Locate every uninfected red blood cell.
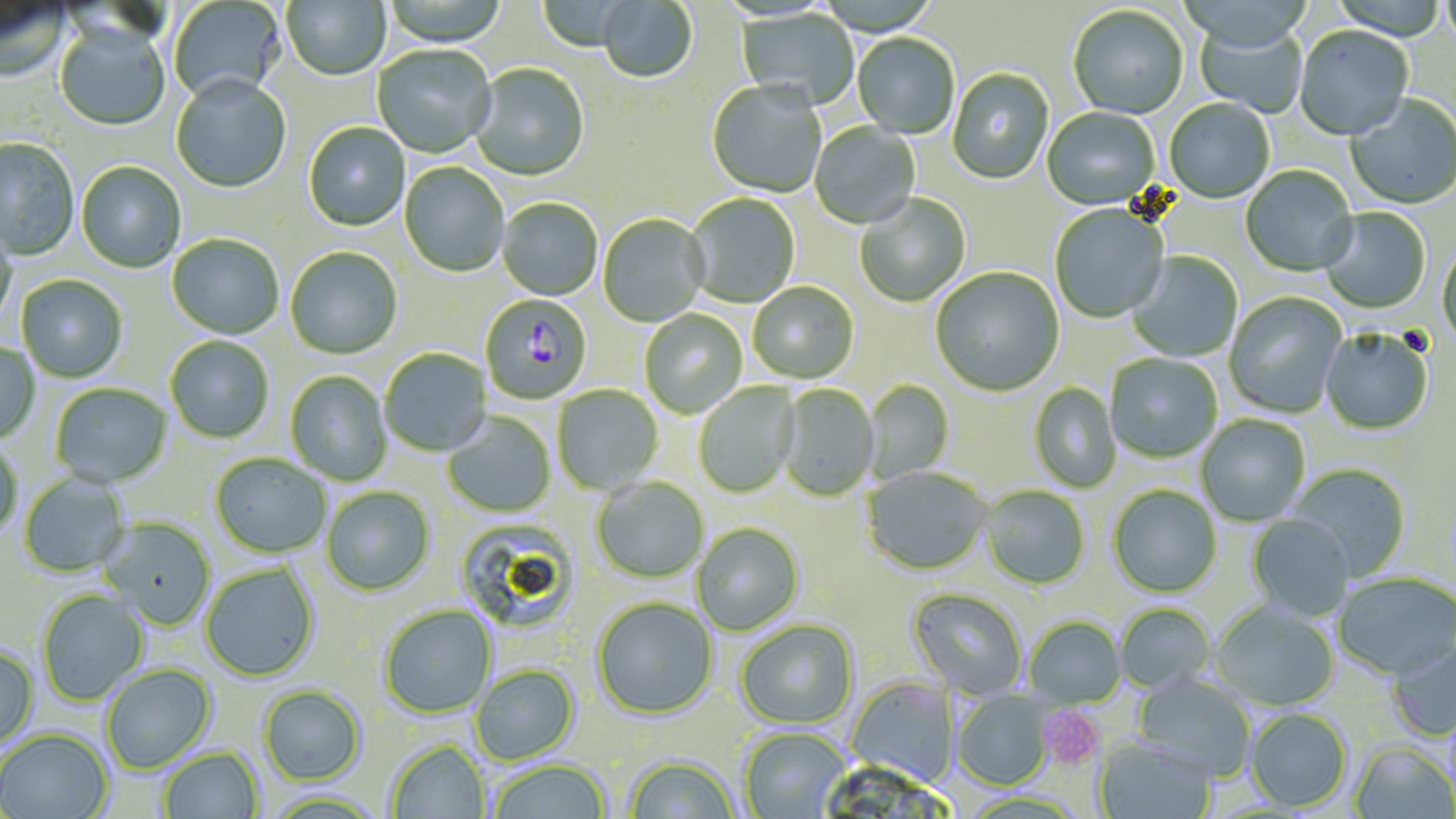

Approximate bounding boxes as (x1,y1)-(x2,y2) corner pairs in pixels.
Uninfected red blood cells: (281,0)-(390,82), (380,0)-(507,48), (536,0)-(640,53), (1440,0)-(1456,57), (1,1)-(72,84), (167,1)-(287,106), (597,1)-(698,85), (1067,6)-(1189,120), (735,9)-(859,110), (1191,22)-(1309,118), (53,26)-(170,132), (1294,26)-(1413,143), (852,34)-(959,139), (372,46)-(497,159), (469,65)-(589,182), (947,69)-(1054,185), (170,78)-(291,194), (706,82)-(827,199), (1345,95)-(1456,211), (1164,99)-(1275,204), (1042,108)-(1159,211), (809,122)-(921,230), (303,124)-(409,232), (0,139)-(79,262), (76,163)-(186,273), (400,163)-(509,277), (1240,167)-(1359,277), (684,194)-(800,309), (854,194)-(971,308), (497,199)-(602,301), (1050,205)-(1169,324), (1319,208)-(1431,314), (597,214)-(709,327), (0,220)-(17,327), (167,235)-(284,340), (1437,244)-(1456,351), (285,247)-(402,360), (1126,252)-(1242,363), (930,268)-(1064,397), (16,275)-(128,383), (748,282)-(859,384), (1224,292)-(1347,419), (639,309)-(747,418), (1320,329)-(1434,436), (164,336)-(274,444), (0,339)-(42,445), (379,348)-(491,457), (1104,353)-(1222,464), (285,371)-(393,486), (863,380)-(955,483), (693,382)-(800,498), (50,383)-(172,488), (1028,383)-(1121,493), (552,384)-(664,495), (777,384)-(880,501), (443,412)-(555,517), (1196,415)-(1310,526), (0,436)-(24,543), (210,453)-(331,558), (1289,464)-(1411,580), (861,466)-(991,575), (18,472)-(130,577), (592,478)-(709,583), (980,485)-(1090,589), (1108,485)-(1222,598), (321,486)-(435,596), (1246,515)-(1354,621), (98,516)-(216,630), (454,519)-(579,633), (691,523)-(804,635), (199,563)-(320,682), (1333,573)-(1455,680), (907,587)-(1028,700), (36,589)-(149,705), (592,596)-(718,720), (1210,602)-(1340,712), (379,604)-(497,718), (1114,604)-(1214,694), (1023,616)-(1127,709), (735,619)-(859,729), (1386,637)-(1456,741), (0,643)-(39,749), (100,664)-(217,774), (470,665)-(579,765), (1132,672)-(1256,780), (845,676)-(958,788), (257,685)-(367,786), (952,689)-(1055,791), (1245,708)-(1353,813), (739,727)-(850,818), (0,728)-(115,818), (1094,736)-(1217,819), (385,739)-(491,818), (1350,743)-(1455,819), (158,746)-(263,818), (623,754)-(741,818), (486,758)-(611,819).

Platelet locations: (1038,706)-(1106,771). Plasmodium falciparum-infected red blood cell locations: (477,293)-(590,401). Slide-level diagnosis: Plasmodium falciparum. Light microscopy. Thin blood smear. Captured at 1000x magnification. Image is 1456×819 pixels. May-Grünwald-Giemsa stain. Single field of view.